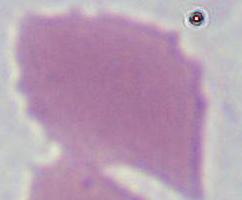
{
  "modality": "photomicrograph",
  "magnification": "1000x",
  "identification": "erythrocyte"
}